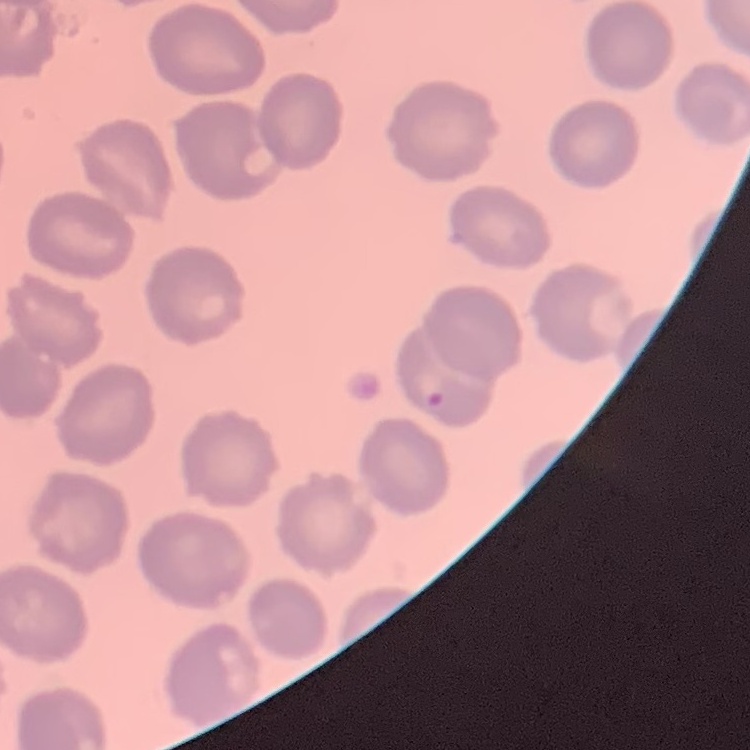
Summary:
  - Erythrocyte morphology: no rouleaux formation
  - Stain: Field's or Giemsa
  - Image type: one tile cut from a larger photomicrograph
  - Preparation: thin blood film